Assess this cell for malaria.
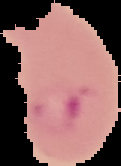

Parasitized.

Summary:
  - Preparation: thin blood film
  - Image size: 121×166 pixels
  - Image type: segmented cell region with the area outside set to black